Give the position of every malaria parasite.
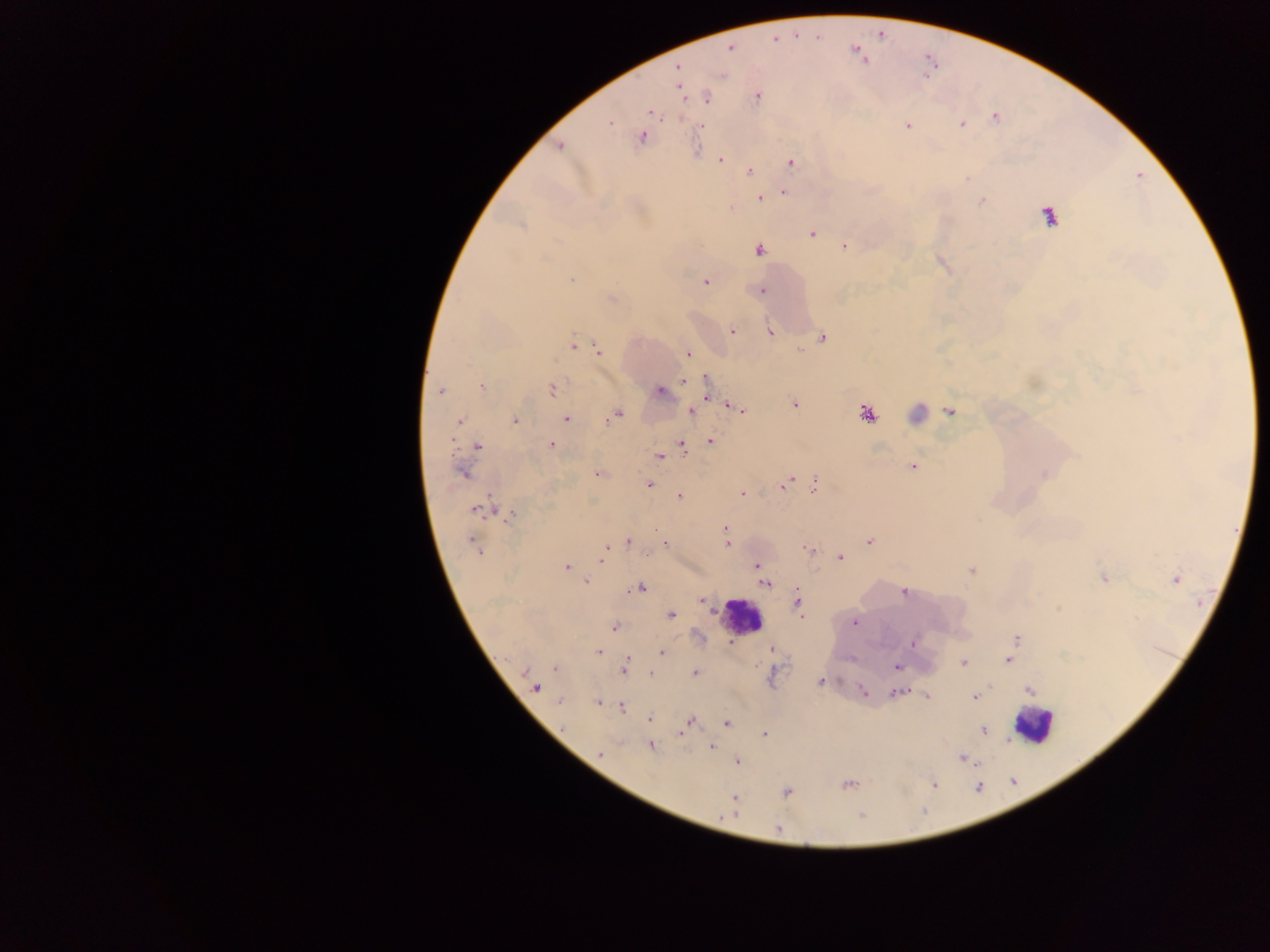
Approximate centers as x y in pixels.
Malaria parasites: 730 48; 678 68; 679 89; 756 96; 707 98; 650 112; 996 117; 609 123; 962 124; 907 126; 642 137; 559 146; 720 159; 791 162; 750 172; 783 192; 761 199; 982 200; 732 208; 1049 216; 521 225; 812 234; 844 246; 758 250; 571 279; 705 282; 761 291; 612 299; 732 331; 770 332; 822 338; 573 343; 599 350; 688 354; 706 380; 685 381; 481 387; 552 389; 440 390; 660 391; 794 405; 697 408; 738 408; 950 410; 692 411; 867 413; 615 415; 566 419; 460 421; 515 421; 710 442; 551 444; 478 446; 682 447; 660 457; 913 466; 463 474; 598 474; 1045 475; 787 483; 649 484; 814 485; 742 493; 679 496; 476 509; 510 515; 726 529; 628 541; 870 541; 473 543; 665 544; 727 545; 606 548; 808 549; 840 557; 601 559; 757 565; 567 567; 971 570; 1104 579; 1176 579; 586 582; 765 583; 640 588; 904 593; 798 601; 702 602; 671 616; 854 623; 613 627; 1017 639; 732 643; 912 643; 772 650; 598 652; 661 652; 1009 660; 964 663; 897 666; 555 667; 624 670; 651 673; 695 673; 819 682; 534 688; 1029 690; 863 691; 896 693; 927 697; 975 697; 559 702; 598 703; 621 707; 649 720; 726 722; 688 723; 685 728; 983 730; 681 732; 765 734; 651 746; 711 747; 600 753; 963 759; 737 762; 849 785; 934 785; 787 793; 734 798; 730 816; 778 828.

preparation = thick blood smear
leukocyte locations = approximate centers as x y in pixels: 741 615; 1033 726
field of view = single
image size = 1270×952 pixels
capture = mobile-phone photograph through a microscope
country = Ghana